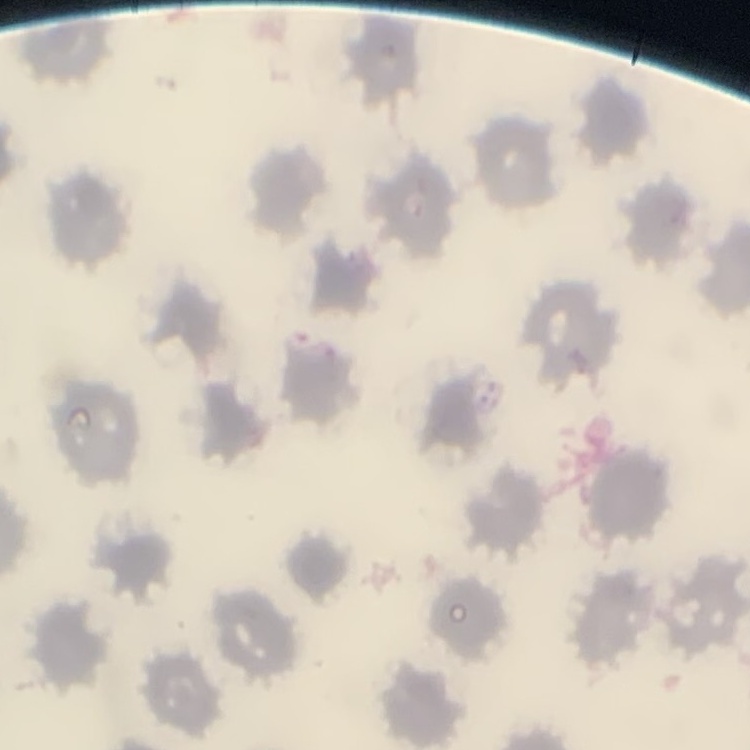
The erythrocytes show no rouleaux formation. Thin peripheral smear. Field's or Giemsa stain. One tile cut from a larger photomicrograph.